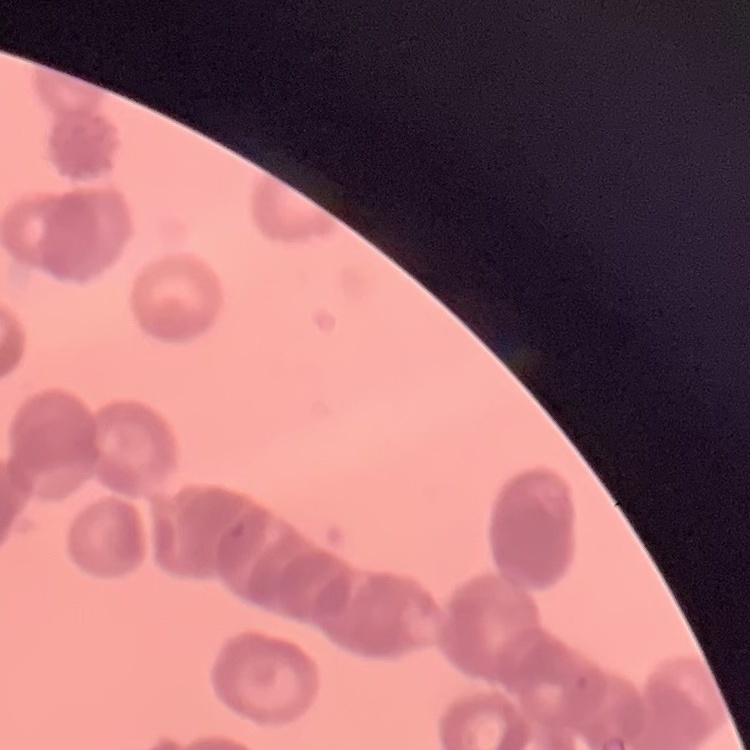

{
  "erythrocyte_morphology": "rouleaux formation",
  "stain": "Field's or Giemsa",
  "image_type": "one tile cut from a larger photomicrograph",
  "preparation": "thin peripheral smear"
}